Report the malaria status of this cell.
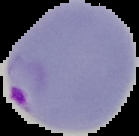
Parasitized.

Image is 139×136 pixels. From a thin blood smear. Segmented cell region on a black background.